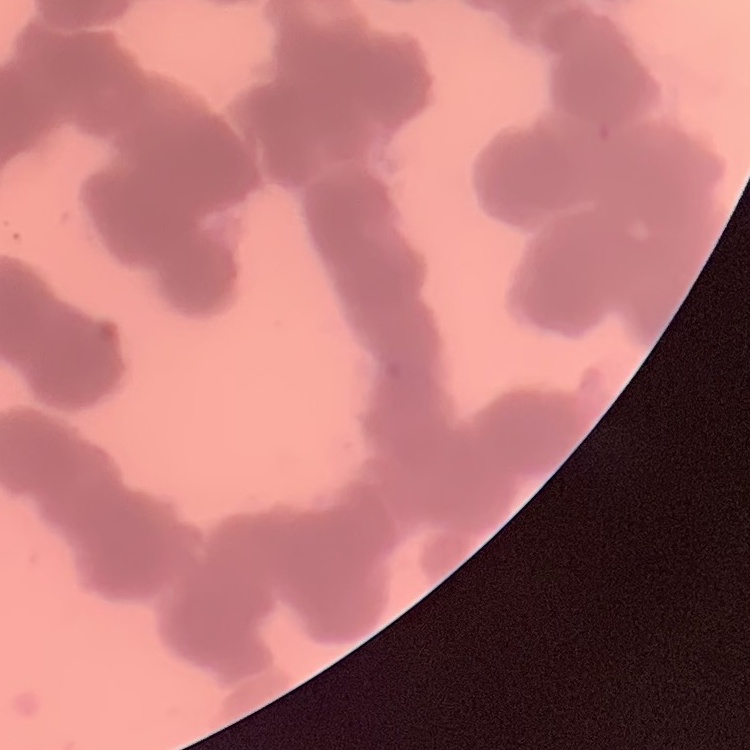

erythrocyte morphology = rouleaux formation
stain = Field's or Giemsa
preparation = thin blood smear
image type = square crop of a larger photomicrograph